Classify this cell by malaria status.
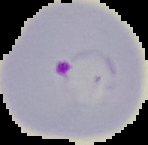

It is parasitized.

image type = segmented cell region with the area outside set to black
image size = 148×145 pixels
preparation = thin blood film